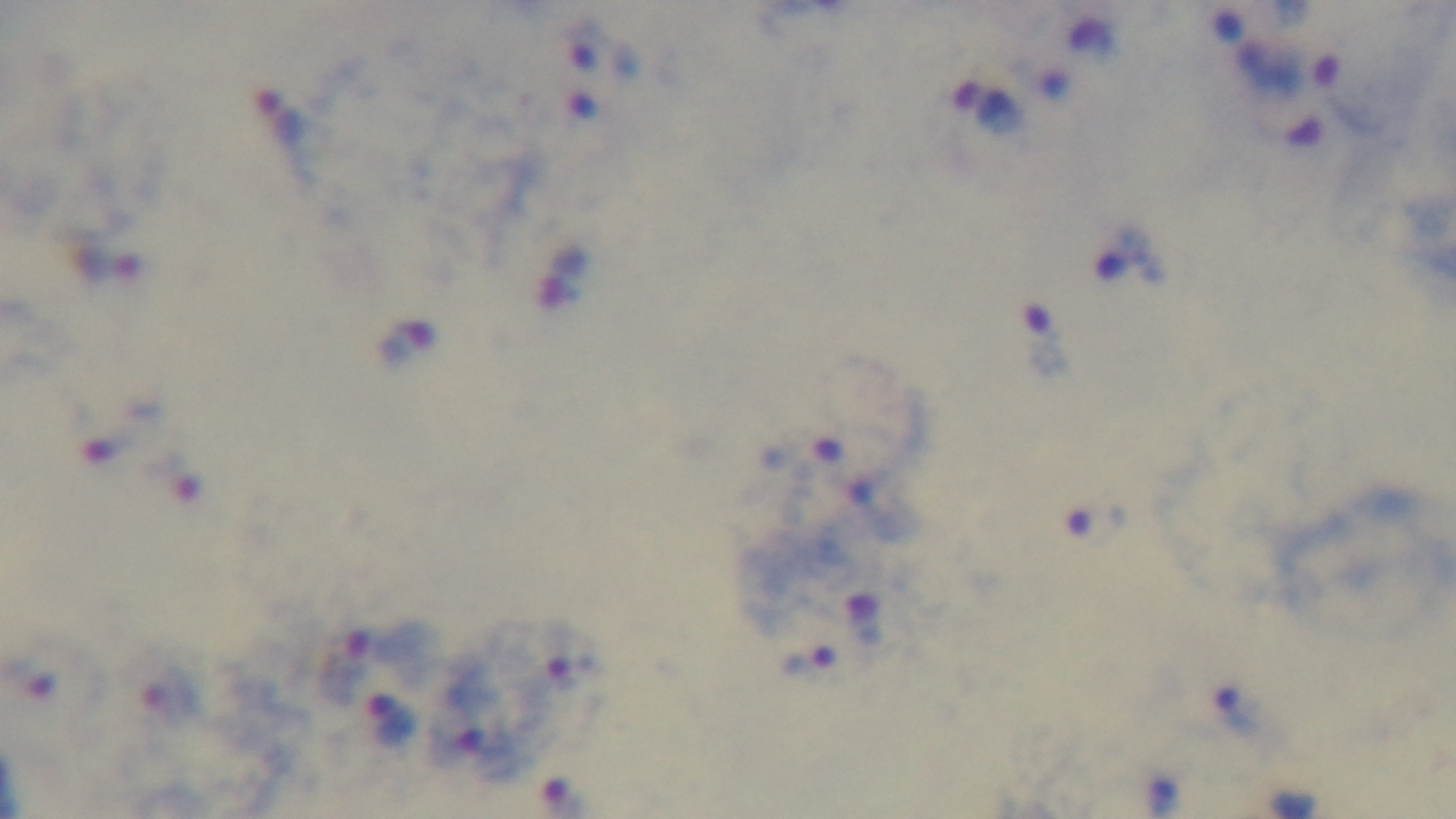 Captured with a mounted 4K digital camera. Preparation: thick smear. Malaria status: infected. Single field of view. Giemsa-stained. Photomicrograph. 100x oil-immersion objective.